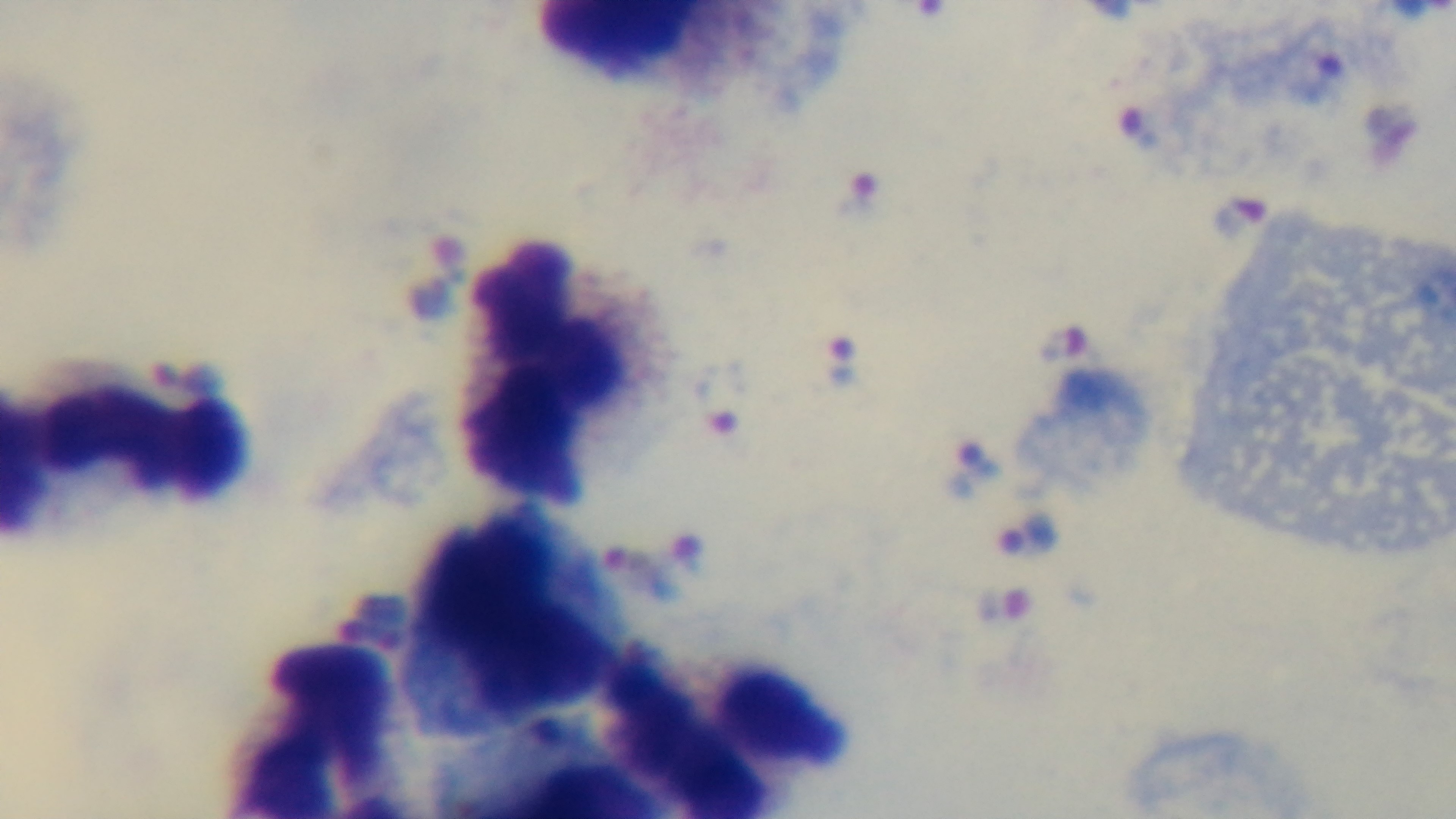
{
  "malaria_status": "infected",
  "field_of_view": "one from the slide",
  "preparation": "thick blood film",
  "objective": "100x oil immersion",
  "modality": "light microscopy",
  "capture": "mounted 4K digital camera",
  "stain": "Giemsa"
}